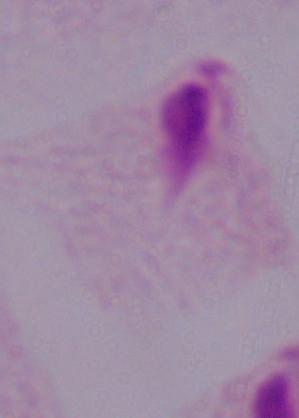 1000x magnification. Micrograph. A trichomonad is shown.